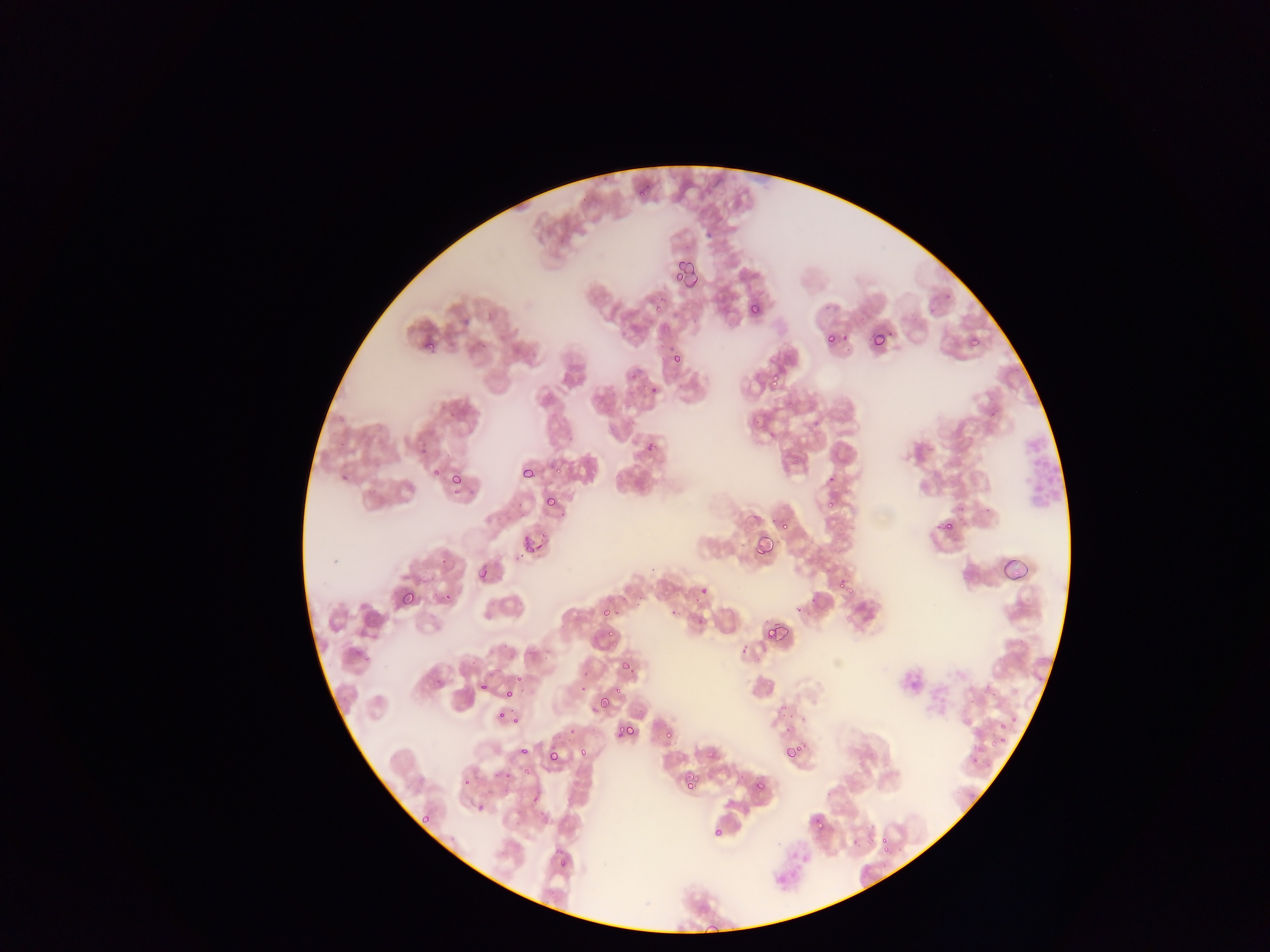

{
  "plasmodium_parasite_locations": "approximate bounding boxes as (left, top, right, bottom) in pixels: (679, 262, 698, 283), (749, 304, 759, 314), (870, 331, 886, 349), (825, 333, 836, 343), (419, 336, 434, 350), (968, 336, 979, 345), (423, 340, 435, 351), (671, 352, 682, 364), (627, 370, 638, 380), (766, 371, 782, 388), (649, 385, 658, 394), (990, 410, 999, 418), (643, 438, 658, 452), (433, 466, 443, 476), (521, 467, 537, 481), (443, 468, 462, 484), (340, 473, 349, 482), (450, 473, 462, 485), (825, 473, 837, 486), (545, 495, 557, 507), (826, 499, 837, 509), (939, 517, 955, 533), (776, 518, 791, 533), (753, 534, 774, 557), (525, 537, 541, 555), (476, 565, 488, 579), (838, 579, 855, 597), (398, 586, 416, 606), (698, 586, 708, 595), (443, 591, 454, 602), (600, 608, 609, 617), (669, 609, 679, 618), (763, 622, 781, 641), (601, 628, 618, 641), (619, 660, 629, 669), (479, 682, 489, 692), (505, 689, 517, 701), (596, 696, 612, 711), (496, 710, 506, 720), (514, 715, 522, 725), (618, 723, 633, 736), (662, 727, 674, 741), (783, 744, 801, 760), (517, 746, 528, 756), (578, 748, 587, 758), (706, 748, 717, 759), (548, 750, 559, 762), (523, 768, 532, 776), (685, 773, 698, 785), (461, 778, 469, 786), (683, 778, 696, 789), (754, 781, 765, 792), (475, 802, 484, 811), (421, 814, 431, 824), (813, 818, 825, 830), (712, 826, 724, 838), (879, 836, 888, 847), (879, 839, 891, 849), (559, 857, 570, 867), (702, 925, 724, 936)",
  "field_of_view": "single",
  "leukocyte_locations": "approximate bounding boxes as (left, top, right, bottom) in pixels: (1018, 427, 1062, 511)",
  "country": "Ghana",
  "preparation": "thin blood film",
  "capture": "mobile-phone photograph through a microscope",
  "image_size": "1270×952 pixels"
}